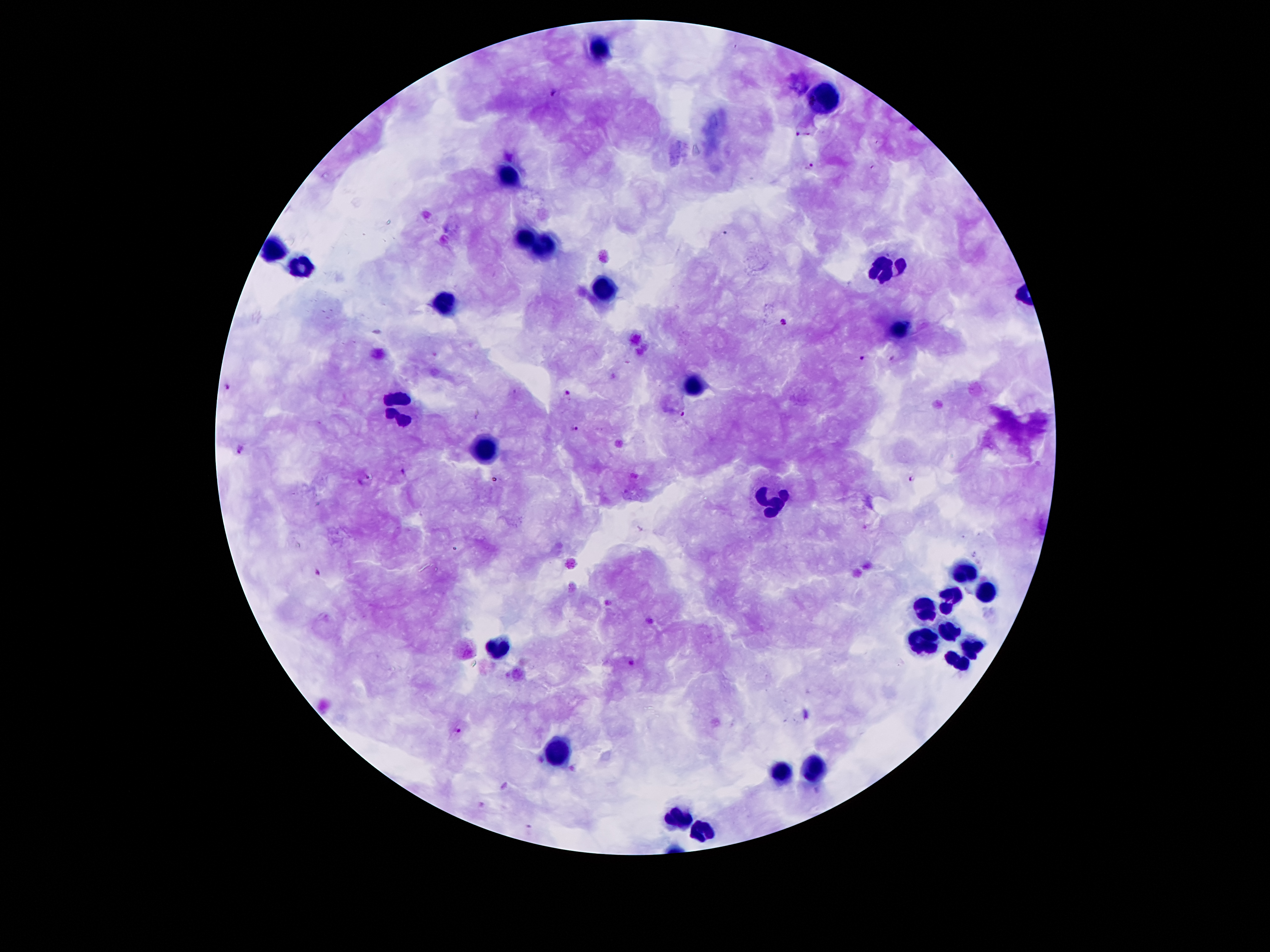
Approximate object centers, in pixels from the top-left corner.
Summary:
  - Plasmodium parasite locations: (x=555, y=93), (x=801, y=136), (x=810, y=167), (x=725, y=233), (x=784, y=321), (x=861, y=358), (x=228, y=387), (x=566, y=393), (x=682, y=413), (x=572, y=428), (x=241, y=450), (x=404, y=472), (x=911, y=478), (x=364, y=479), (x=317, y=572), (x=632, y=662), (x=458, y=730), (x=531, y=828)
  - Leukocyte locations: (x=605, y=44), (x=824, y=99), (x=511, y=178), (x=530, y=239), (x=544, y=246), (x=275, y=252), (x=303, y=264), (x=887, y=269), (x=605, y=294), (x=448, y=308), (x=899, y=330), (x=693, y=383), (x=396, y=408), (x=485, y=446), (x=780, y=507), (x=966, y=575), (x=986, y=594), (x=949, y=600), (x=921, y=609), (x=948, y=634), (x=925, y=643), (x=508, y=646), (x=976, y=649), (x=961, y=666), (x=561, y=754), (x=818, y=770), (x=783, y=772), (x=682, y=821), (x=701, y=834)
  - Patient malaria status: infected with Plasmodium falciparum
  - Field of view: one from this slide
  - Capture: smartphone through the microscope eyepiece
  - Preparation: thick peripheral-blood smear
  - Magnification: 100x
  - Image size: 1270×952 pixels
  - Stain: Giemsa